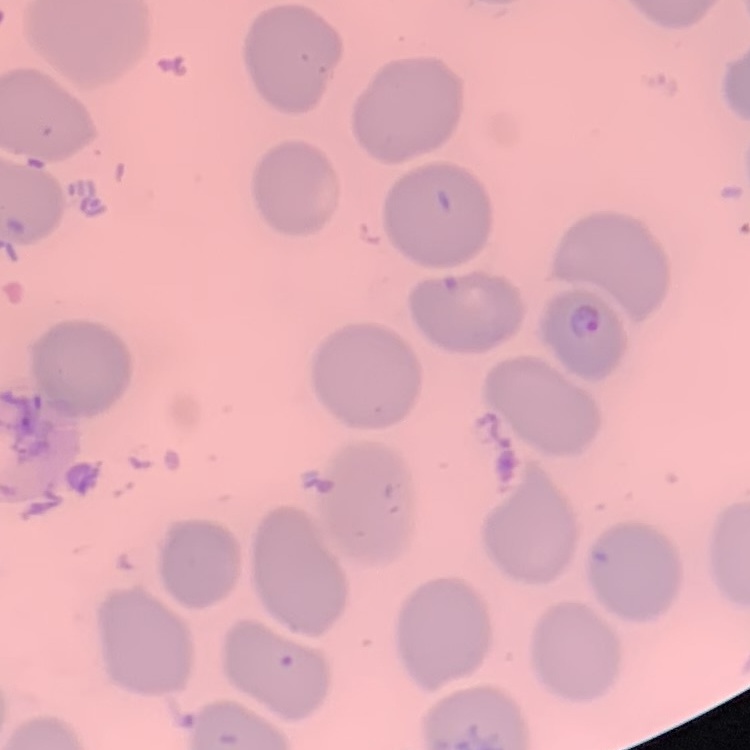
Summary:
  - Erythrocyte morphology: no rouleaux formation
  - Preparation: thin blood film
  - Stain: Field's or Giemsa
  - Image type: square crop of a larger photomicrograph